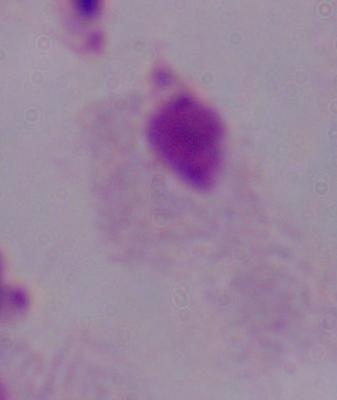
Summary:
  - Identification: trichomonad
  - Magnification: 1000x
  - Modality: micrograph